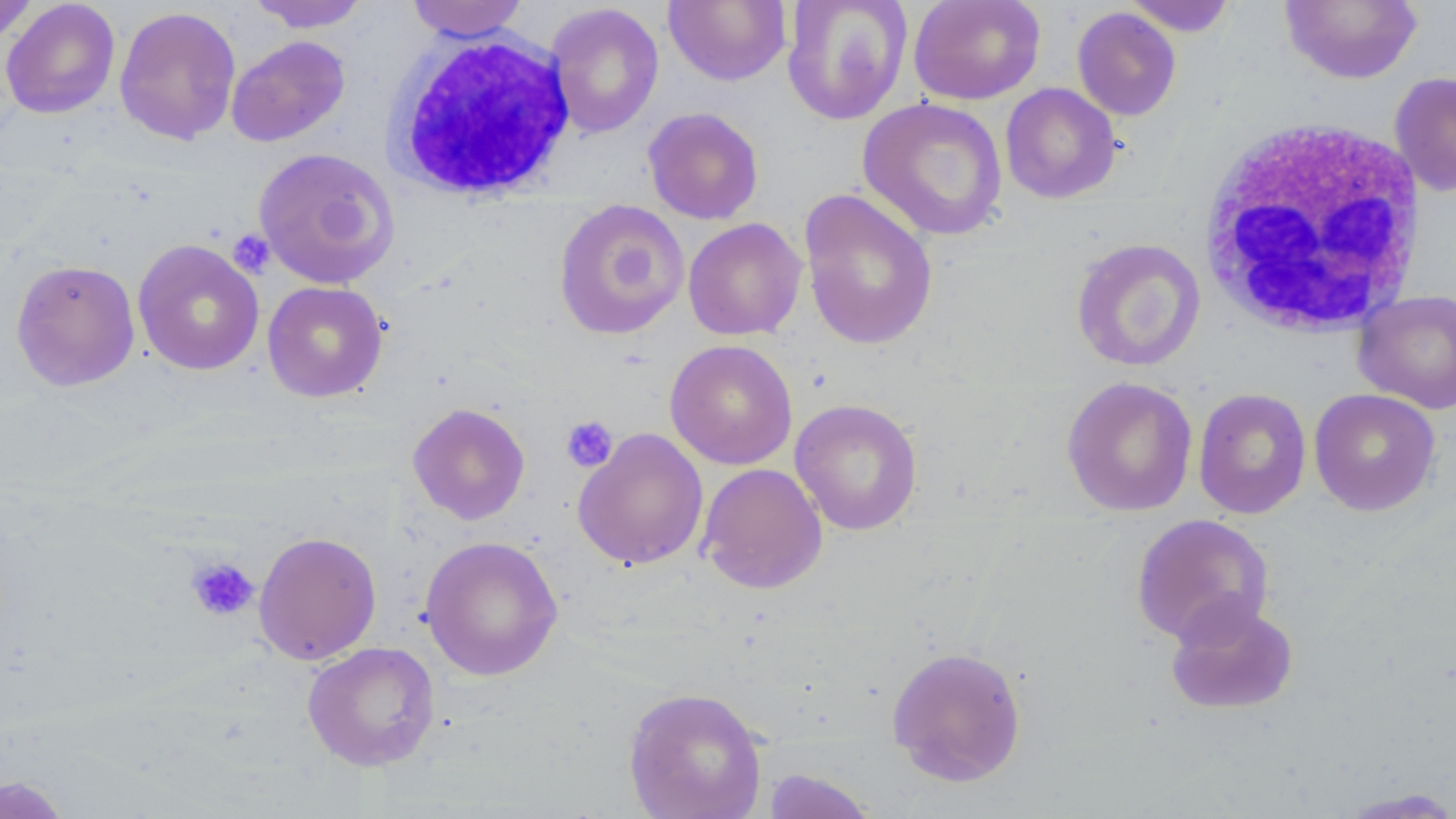

Summary:
  - Coordinate format: approximate bounding boxes as (x1, y1, x2, y2) in pixels
  - Platelet locations: (228, 230, 274, 276), (560, 415, 618, 473), (186, 556, 259, 622)
  - Uninfected red blood cell locations: (0, 0, 38, 47), (1, 0, 120, 119), (248, 0, 370, 32), (405, 0, 530, 42), (664, 0, 791, 86), (782, 0, 912, 125), (908, 0, 1046, 105), (1121, 0, 1238, 36), (1280, 0, 1423, 85), (545, 3, 664, 138), (114, 6, 241, 146), (1072, 7, 1182, 121), (226, 35, 350, 147), (1389, 71, 1456, 197), (1000, 83, 1121, 204), (858, 97, 1008, 241), (643, 107, 764, 225), (252, 147, 400, 289), (798, 188, 939, 351), (554, 199, 690, 340), (683, 218, 807, 341), (1071, 238, 1206, 372), (132, 239, 265, 376), (11, 259, 140, 391), (262, 281, 388, 402), (1353, 289, 1456, 414), (664, 339, 797, 470), (1061, 376, 1198, 517), (1193, 388, 1312, 519), (1308, 388, 1441, 516), (790, 398, 923, 536), (407, 403, 530, 525), (572, 428, 709, 570), (698, 462, 828, 594), (1131, 513, 1274, 646), (253, 531, 382, 665), (420, 535, 563, 681), (1164, 596, 1299, 715), (302, 641, 440, 771), (887, 645, 1027, 787), (623, 687, 768, 819), (761, 769, 879, 818), (0, 775, 72, 818), (1336, 786, 1456, 818)
  - White blood cell locations: (385, 30, 577, 202), (1197, 116, 1430, 339)
  - Slide-level diagnosis: no evidence of blood parasites
  - Modality: light microscopy
  - Field of view: one of a larger specimen
  - Preparation: thin blood film
  - Stain: May-Grünwald-Giemsa
  - Magnification: 1000x
  - Image size: 1456×819 pixels